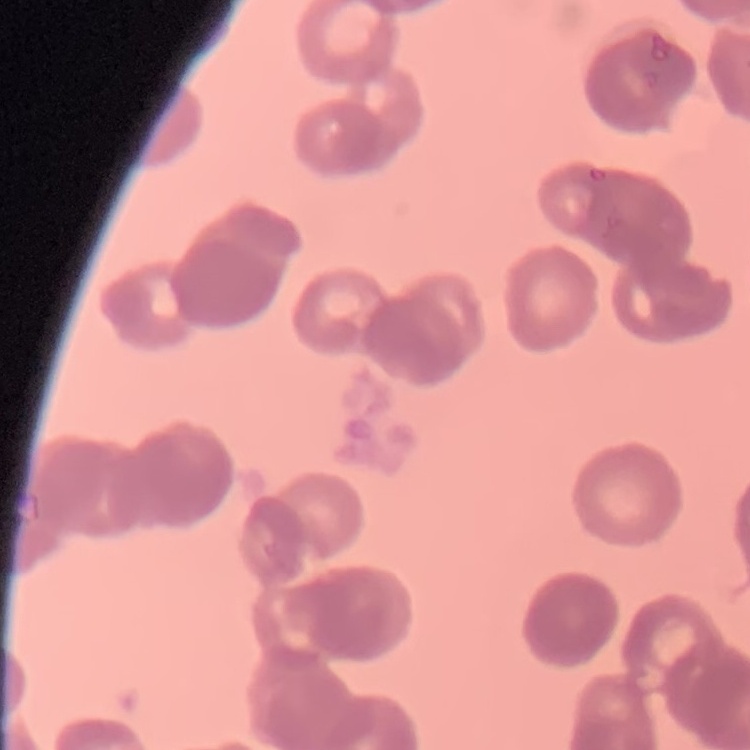

red blood cell morphology = rouleaux formation
stain = Field's or Giemsa
preparation = thin peripheral smear
image type = one tile cut from a larger photomicrograph